Assess this cell for malaria.
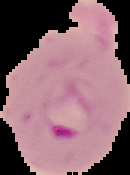
Parasitized.

image size = 130×175 pixels
image type = segmented cell region with the area outside set to black
preparation = thin blood film